Locate platelets.
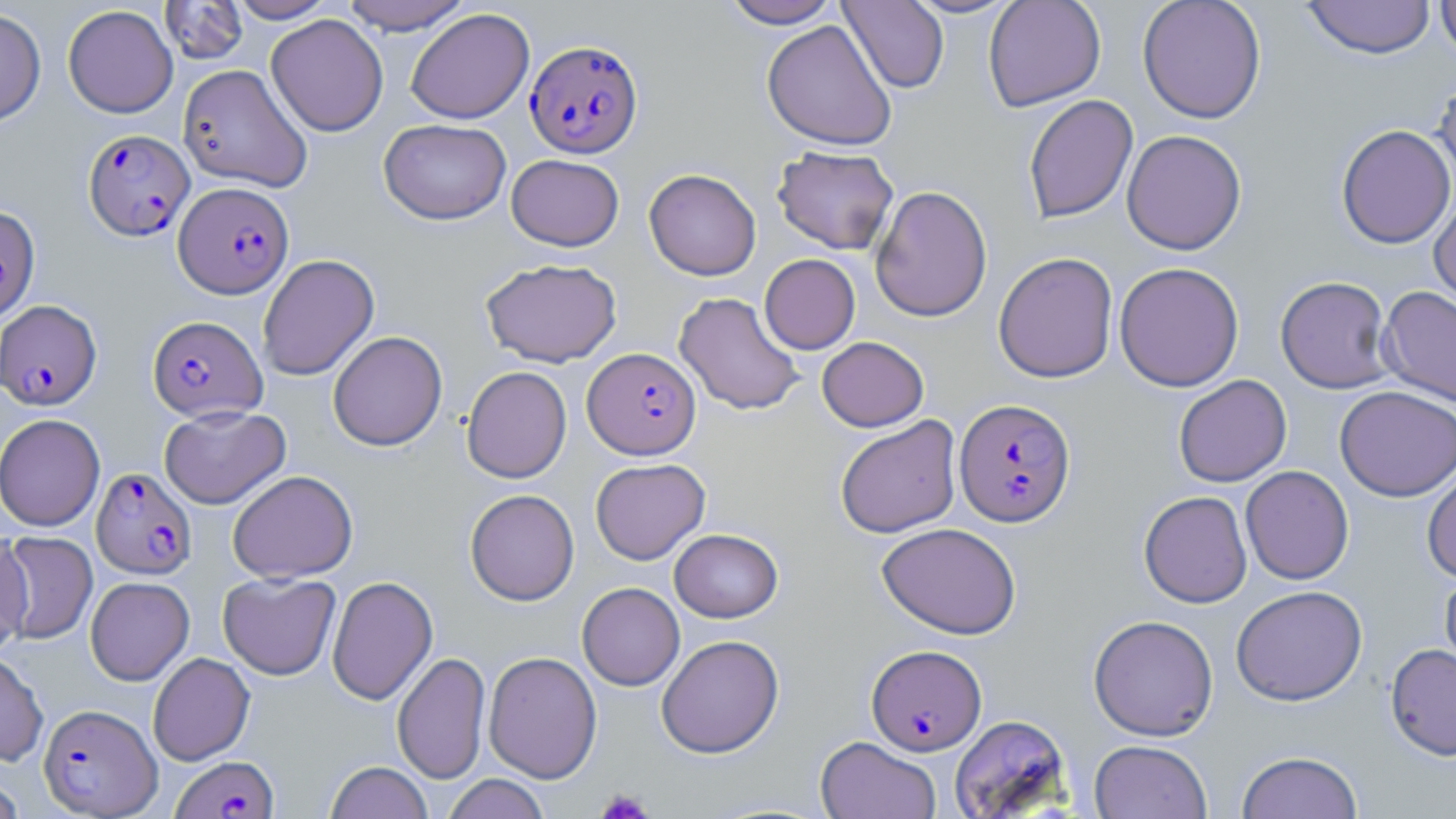

Approximate bounding boxes as (x1,y1)-(x2,y2) corner pairs in pixels.
Platelets: (595,788)-(654,818).

Summary:
  - Plasmodium falciparum-infected red blood cell locations: (526,39)-(643,158), (83,129)-(195,241), (173,181)-(293,298), (0,300)-(103,411), (147,315)-(267,421), (583,347)-(701,459), (954,398)-(1076,527), (91,467)-(197,579), (866,644)-(986,755), (39,703)-(161,817), (171,755)-(279,818)
  - Uninfected red blood cell locations: (159,0)-(249,65), (225,0)-(338,23), (340,0)-(472,35), (721,0)-(843,28), (901,0)-(1022,19), (983,0)-(1106,112), (1137,0)-(1266,124), (1302,0)-(1436,59), (1435,0)-(1456,61), (838,1)-(949,93), (62,4)-(178,118), (0,7)-(46,127), (405,8)-(534,124), (266,14)-(388,137), (761,20)-(897,151), (178,64)-(313,192), (1433,74)-(1456,195), (1023,94)-(1138,224), (378,118)-(511,225), (1335,124)-(1455,249), (1122,129)-(1247,256), (772,145)-(899,255), (506,154)-(624,251), (644,169)-(761,280), (870,185)-(993,322), (1429,192)-(1456,310), (0,204)-(41,324), (993,251)-(1118,383), (257,254)-(379,381), (759,254)-(860,354), (480,258)-(622,367), (1114,261)-(1244,391), (1275,276)-(1395,393), (1378,286)-(1456,407), (674,292)-(805,416), (327,331)-(448,451), (817,336)-(929,432), (461,366)-(572,483), (1174,374)-(1292,487), (1334,385)-(1456,501), (159,404)-(290,509), (0,413)-(105,532), (835,415)-(962,538), (590,458)-(710,564), (1422,464)-(1456,583), (1240,465)-(1354,585), (228,469)-(358,583), (465,489)-(579,605), (1139,490)-(1252,608), (877,522)-(1021,639), (669,528)-(783,622), (0,531)-(33,655), (1,532)-(98,644), (1439,569)-(1456,683), (217,572)-(341,680), (327,575)-(438,705), (85,576)-(194,685), (577,582)-(685,691), (1231,585)-(1368,706), (1088,614)-(1219,741), (656,634)-(784,758), (1386,643)-(1456,760), (0,649)-(48,767), (392,651)-(490,784), (483,651)-(602,783), (148,652)-(255,765), (949,714)-(1072,817), (815,736)-(941,819), (1089,739)-(1212,819), (1236,750)-(1363,819), (325,761)-(433,819), (441,774)-(551,819), (0,775)-(27,818)
  - Slide-level diagnosis: Plasmodium falciparum
  - Modality: light microscopy
  - Stain: May-Grünwald-Giemsa
  - Magnification: 1000x
  - Field of view: one of a larger specimen
  - Image size: 1456×819 pixels
  - Preparation: thin blood film